Evaluate for malaria.
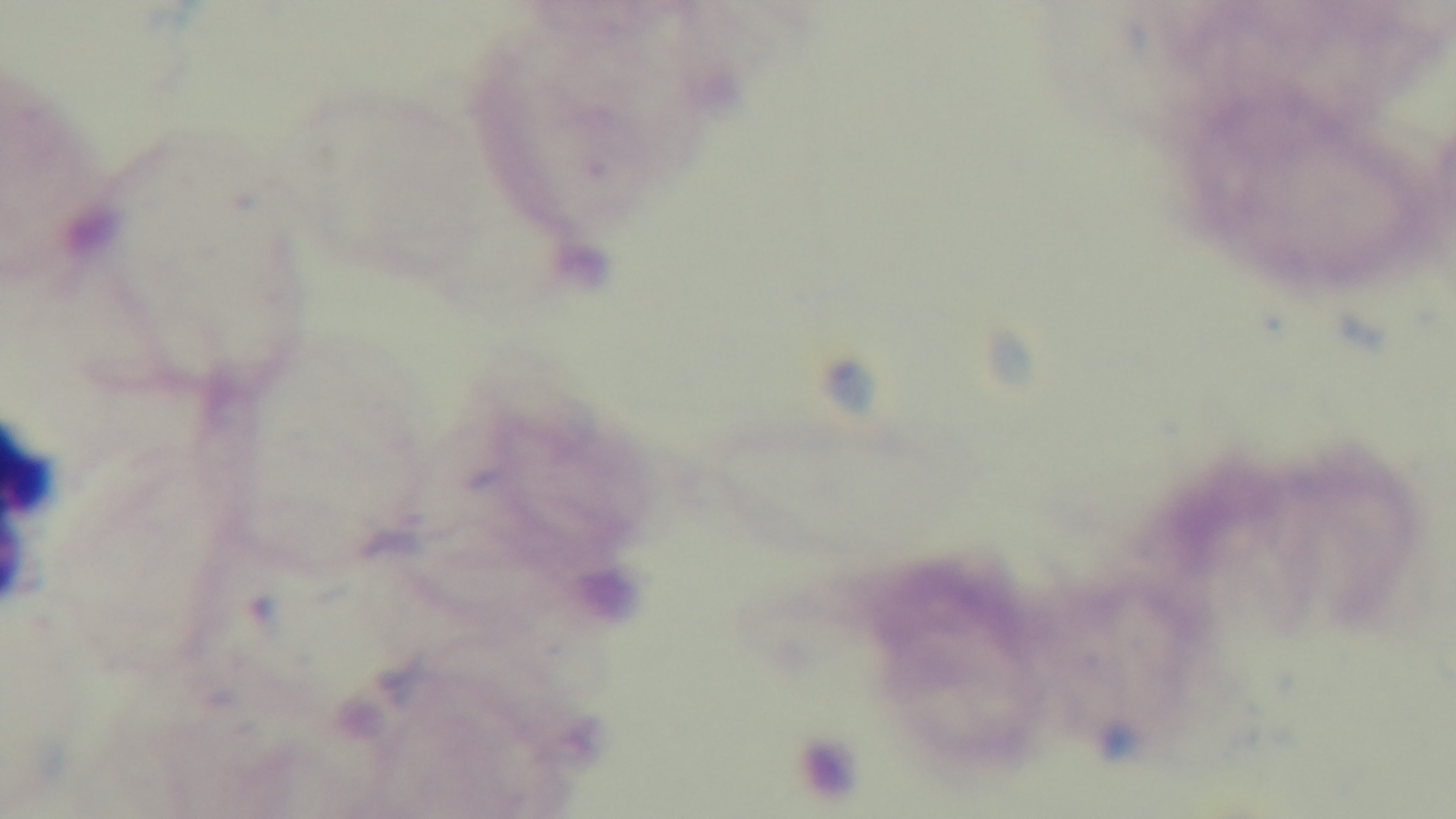
Uninfected.

Preparation: thick smear. Photomicrograph. Oil-immersion objective, 100x. Mounted 4K digital camera. Single field of view. Giemsa-stained.